State the blood parasite species.
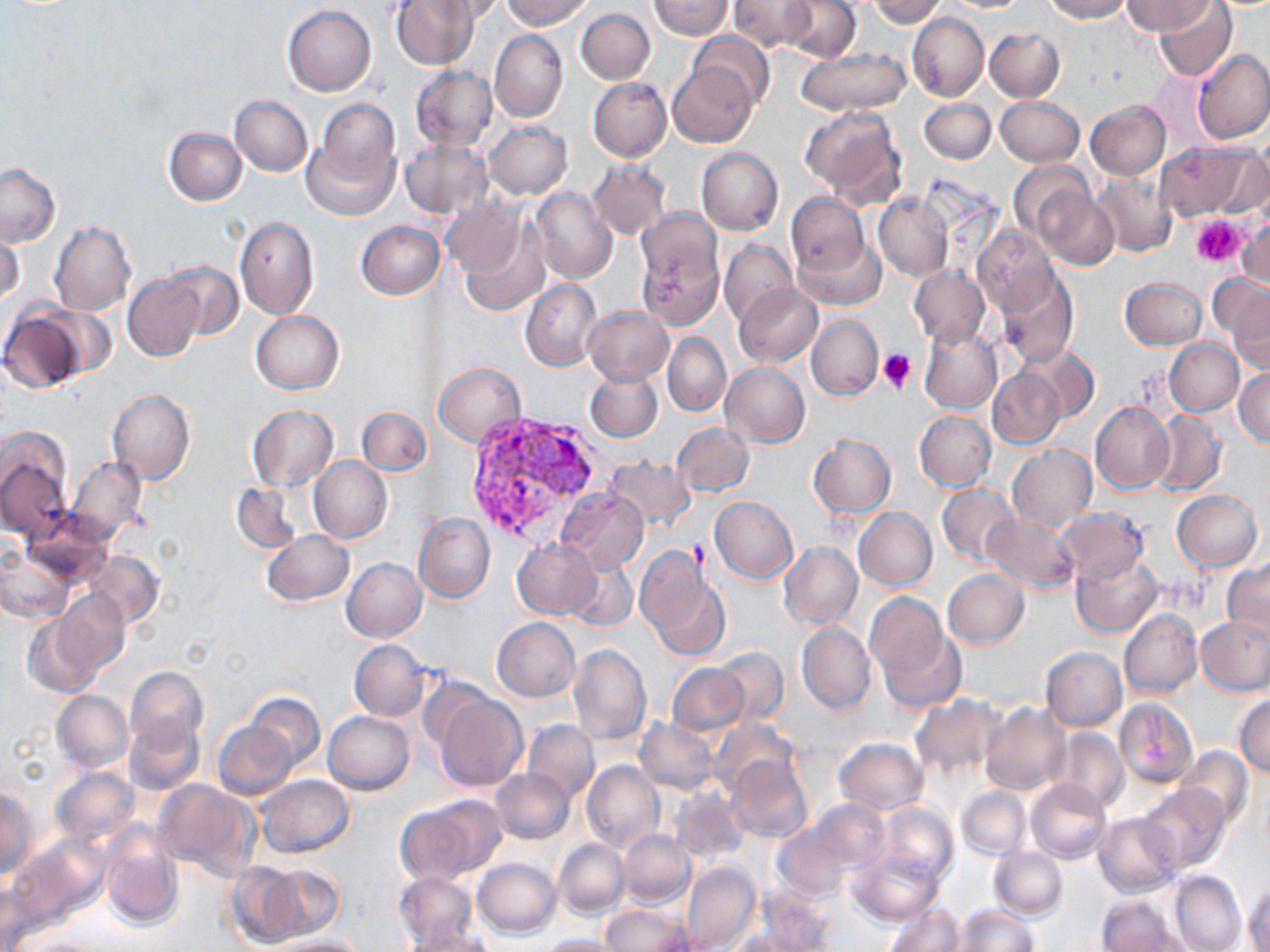
Plasmodium vivax.

Approximate bounding boxes as [x1, y1, x2, y2] in pixels. Uninfected red blood cell locations: [391, 0, 480, 70], [432, 0, 507, 22], [502, 0, 593, 29], [650, 0, 733, 40], [780, 0, 862, 62], [868, 0, 946, 26], [1043, 0, 1129, 22], [1123, 0, 1213, 35], [1154, 0, 1236, 81], [728, 1, 815, 51], [282, 5, 377, 96], [575, 7, 655, 85], [907, 13, 988, 102], [984, 29, 1065, 102], [488, 30, 567, 122], [688, 31, 774, 110], [795, 47, 911, 117], [1193, 50, 1270, 145], [668, 61, 758, 148], [409, 66, 496, 153], [587, 78, 671, 161], [230, 95, 313, 176], [994, 97, 1084, 168], [919, 99, 996, 164], [1086, 100, 1171, 181], [303, 101, 403, 221], [797, 107, 907, 203], [484, 121, 572, 199], [164, 127, 247, 206], [399, 141, 490, 217], [1203, 143, 1270, 220], [1155, 144, 1249, 222], [695, 148, 783, 237], [588, 161, 671, 240], [1008, 161, 1095, 239], [0, 164, 61, 248], [1091, 173, 1179, 258], [1035, 186, 1121, 269], [528, 188, 617, 283], [873, 194, 952, 282], [785, 195, 869, 276], [441, 196, 527, 281], [632, 213, 726, 327], [234, 216, 319, 319], [1235, 219, 1269, 291], [355, 221, 442, 300], [49, 222, 137, 316], [456, 224, 551, 318], [1, 225, 24, 307], [972, 228, 1056, 316], [794, 234, 884, 309], [718, 240, 796, 325], [162, 261, 243, 342], [909, 267, 989, 348], [997, 268, 1079, 366], [122, 275, 203, 362], [1120, 277, 1208, 350], [520, 279, 603, 371], [1224, 282, 1269, 371], [734, 283, 822, 368], [0, 306, 94, 393], [583, 306, 673, 385], [251, 311, 343, 394], [806, 316, 882, 399], [918, 327, 1002, 414], [662, 333, 731, 417], [1164, 338, 1243, 416], [1019, 346, 1099, 424], [435, 363, 525, 448], [721, 363, 810, 449], [1234, 369, 1269, 445], [584, 371, 662, 442], [988, 371, 1063, 450], [106, 390, 195, 484], [1089, 402, 1174, 494], [246, 405, 337, 492], [356, 406, 430, 475], [914, 411, 996, 491], [1145, 411, 1226, 498], [671, 422, 753, 497], [0, 432, 72, 541], [807, 434, 895, 517], [1007, 445, 1096, 530], [605, 455, 695, 530], [66, 456, 148, 542], [309, 456, 393, 543], [230, 483, 302, 554], [937, 484, 1019, 564], [554, 488, 648, 574], [1171, 490, 1261, 571], [709, 497, 799, 583], [852, 508, 937, 591], [1055, 508, 1147, 583], [413, 514, 494, 604], [983, 514, 1079, 592], [261, 529, 354, 607], [512, 538, 602, 619], [778, 543, 862, 630], [637, 547, 729, 660], [0, 548, 75, 621], [83, 549, 164, 628], [1070, 552, 1163, 637], [341, 558, 427, 643], [564, 558, 638, 631], [1222, 561, 1269, 643], [942, 569, 1029, 647], [55, 589, 128, 676], [865, 593, 948, 686], [1119, 608, 1202, 697], [21, 613, 102, 698], [1196, 617, 1270, 695], [491, 618, 580, 702], [797, 623, 876, 715], [877, 626, 966, 713], [350, 640, 429, 721], [568, 642, 651, 745], [713, 647, 789, 724], [1040, 647, 1127, 731], [666, 663, 749, 736], [124, 665, 208, 753], [51, 690, 133, 773], [245, 691, 324, 771], [430, 691, 528, 792], [909, 693, 1006, 780], [1232, 694, 1270, 776], [1113, 697, 1198, 789], [980, 703, 1070, 795], [324, 711, 414, 793], [124, 713, 203, 795], [708, 718, 800, 796], [522, 719, 598, 803], [636, 719, 717, 794], [213, 721, 299, 800], [1048, 727, 1128, 811], [835, 737, 928, 815], [1177, 747, 1254, 828], [727, 755, 814, 842], [581, 760, 663, 852], [50, 766, 142, 849], [490, 768, 574, 844], [256, 774, 354, 859], [1026, 778, 1112, 864], [155, 779, 258, 880], [1139, 783, 1232, 874], [671, 785, 749, 863], [956, 787, 1030, 858], [0, 788, 37, 879], [398, 798, 502, 883], [809, 798, 890, 872], [877, 803, 958, 882], [1094, 812, 1183, 896], [100, 821, 184, 930], [772, 823, 855, 900], [618, 830, 694, 906], [12, 833, 110, 927], [553, 837, 628, 916], [988, 846, 1068, 920], [850, 850, 944, 924], [472, 858, 560, 938], [226, 861, 310, 945], [681, 861, 761, 952], [255, 862, 344, 942], [394, 871, 478, 948], [1169, 871, 1246, 952], [1244, 884, 1270, 952], [747, 889, 839, 951], [1096, 896, 1183, 951], [885, 902, 964, 952], [602, 903, 691, 952], [953, 904, 1038, 952], [725, 929, 820, 952], [402, 930, 496, 952], [540, 933, 626, 952], [21, 935, 106, 952], [266, 935, 366, 952]. Platelet locations: [1189, 213, 1247, 267], [878, 350, 917, 393]. Plasmodium vivax-infected red blood cell locations: [475, 412, 600, 520]. Captured at 1000x magnification. Light microscopy. Image is 1270×952 pixels. Single field of view. Thin blood smear. May-Grünwald-Giemsa stain.